Locate every leukocyte (white blood cell).
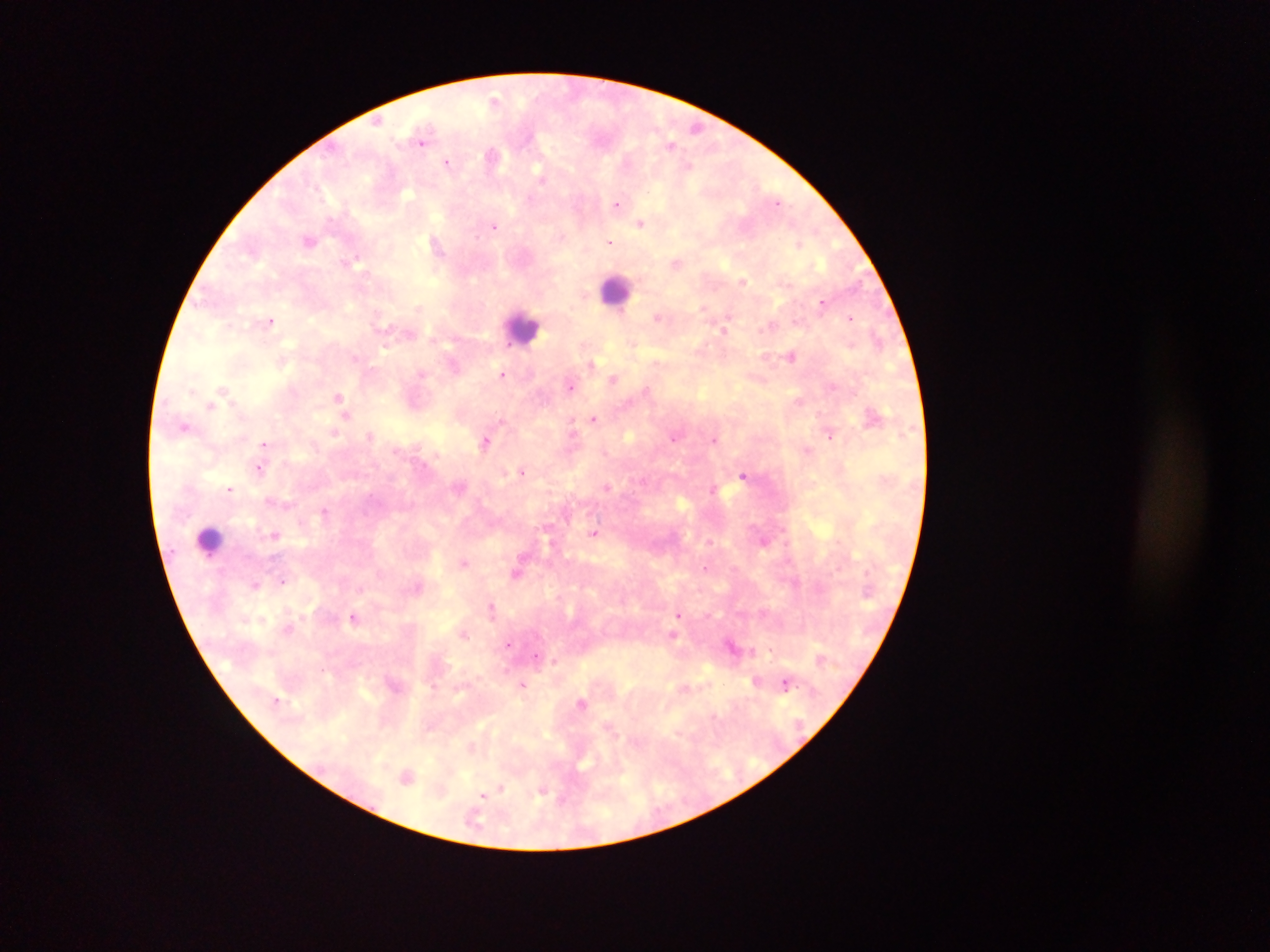

Approximate centers as (x, y) in pixels.
Leukocytes: (616, 291), (524, 328), (210, 541).

Summary:
  - Malaria parasite locations: (494, 100), (377, 122), (696, 127), (422, 142), (671, 144), (491, 155), (446, 161), (690, 165), (542, 178), (778, 202), (617, 204), (642, 223), (494, 227), (563, 236), (309, 240), (610, 242), (800, 244), (437, 246), (356, 259), (677, 263), (744, 281), (822, 302), (703, 307), (657, 318), (850, 318), (271, 321), (769, 327), (723, 330), (877, 338), (510, 344), (633, 344), (385, 347), (792, 356), (355, 358), (592, 364), (453, 366), (421, 373), (502, 374), (614, 379), (570, 386), (832, 387), (222, 389), (646, 389), (338, 397), (209, 408), (346, 415), (594, 419), (572, 425), (184, 426), (334, 432), (370, 436), (830, 436), (674, 437), (714, 439), (484, 442), (264, 444), (807, 449), (259, 468), (523, 471), (744, 476), (607, 487), (230, 489), (713, 489), (324, 511), (594, 533), (274, 535), (463, 562), (705, 568), (517, 574), (282, 581), (254, 584), (418, 586), (492, 608), (679, 614), (353, 617), (672, 635), (509, 644), (731, 645), (770, 650), (536, 655), (554, 661), (785, 683), (523, 684), (581, 703), (407, 776), (500, 788), (542, 792), (482, 796)
  - Preparation: thick blood smear
  - Country: Ghana
  - Field of view: single
  - Capture: mobile-phone photograph through a microscope
  - Image size: 1270×952 pixels